Name the cell type shown.
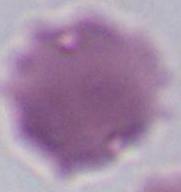
An erythrocyte.

Micrograph. Captured at 1000x magnification.